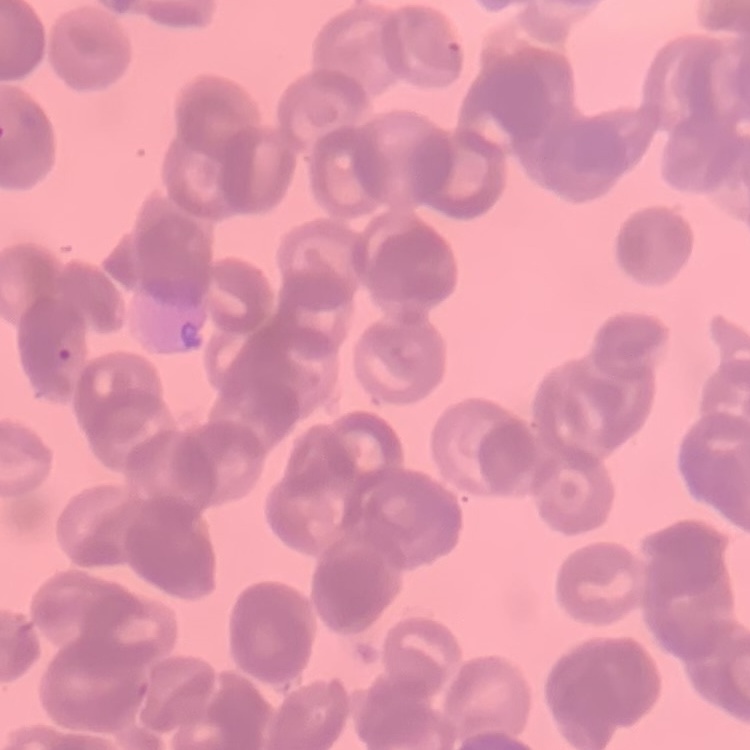
The red blood cells exhibit rouleaux formation. Thin blood film. Square crop of a larger photomicrograph. Field's or Giemsa stain.